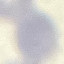

Summary:
  - Result: no malaria parasites detected
  - Image type: automatically extracted cell patch, resized to 64 × 64 pixels
  - Stain: Giemsa
  - Preparation: thin blood film
  - Capture: smartphone through the microscope eyepiece